Point out each Plasmodium parasite.
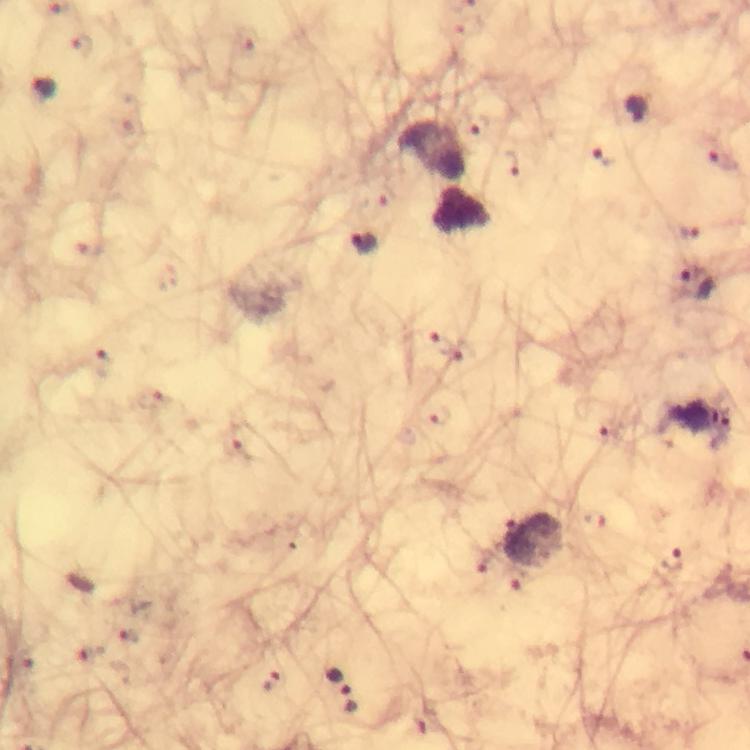
Approximate object centers, in pixels from the top-left corner.
Plasmodium parasites: (x=81, y=46), (x=44, y=89), (x=637, y=111), (x=475, y=127), (x=609, y=156), (x=723, y=162), (x=506, y=165), (x=367, y=243), (x=696, y=285), (x=438, y=344), (x=107, y=364), (x=440, y=416), (x=608, y=429), (x=244, y=449), (x=484, y=560), (x=671, y=561), (x=516, y=580), (x=126, y=636), (x=24, y=661), (x=339, y=680), (x=273, y=684).

A crop from one field of view. From a malaria diagnostic workup. Photographed with a smartphone mounted on the microscope. Giemsa stain. Image is 750×750 pixels. At 100x magnification. Thick blood film. Immersion oil applied.